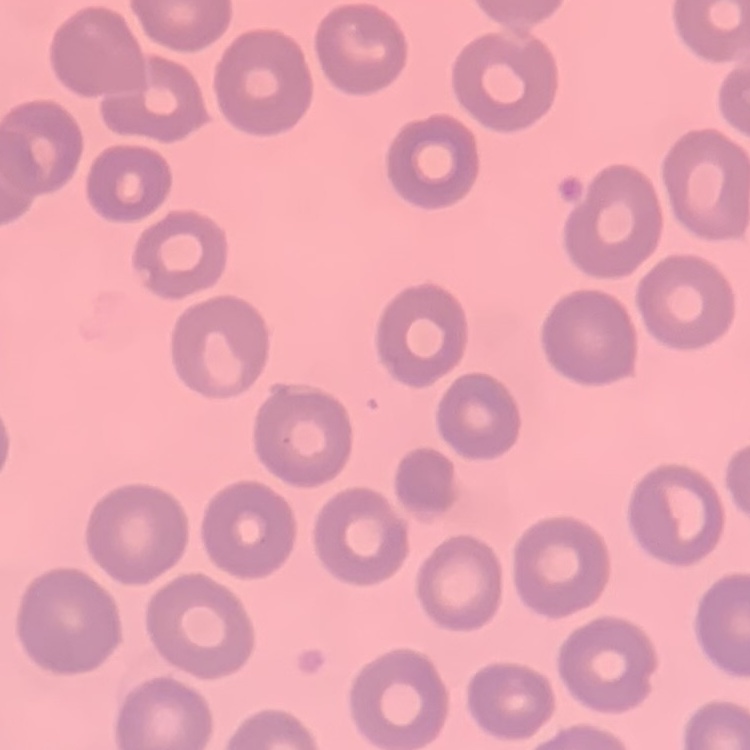

{
  "erythrocyte_morphology": "no rouleaux formation",
  "image_type": "one tile cut from a larger photomicrograph",
  "stain": "Field's or Giemsa",
  "preparation": "thin blood smear"
}